State the blood parasite species.
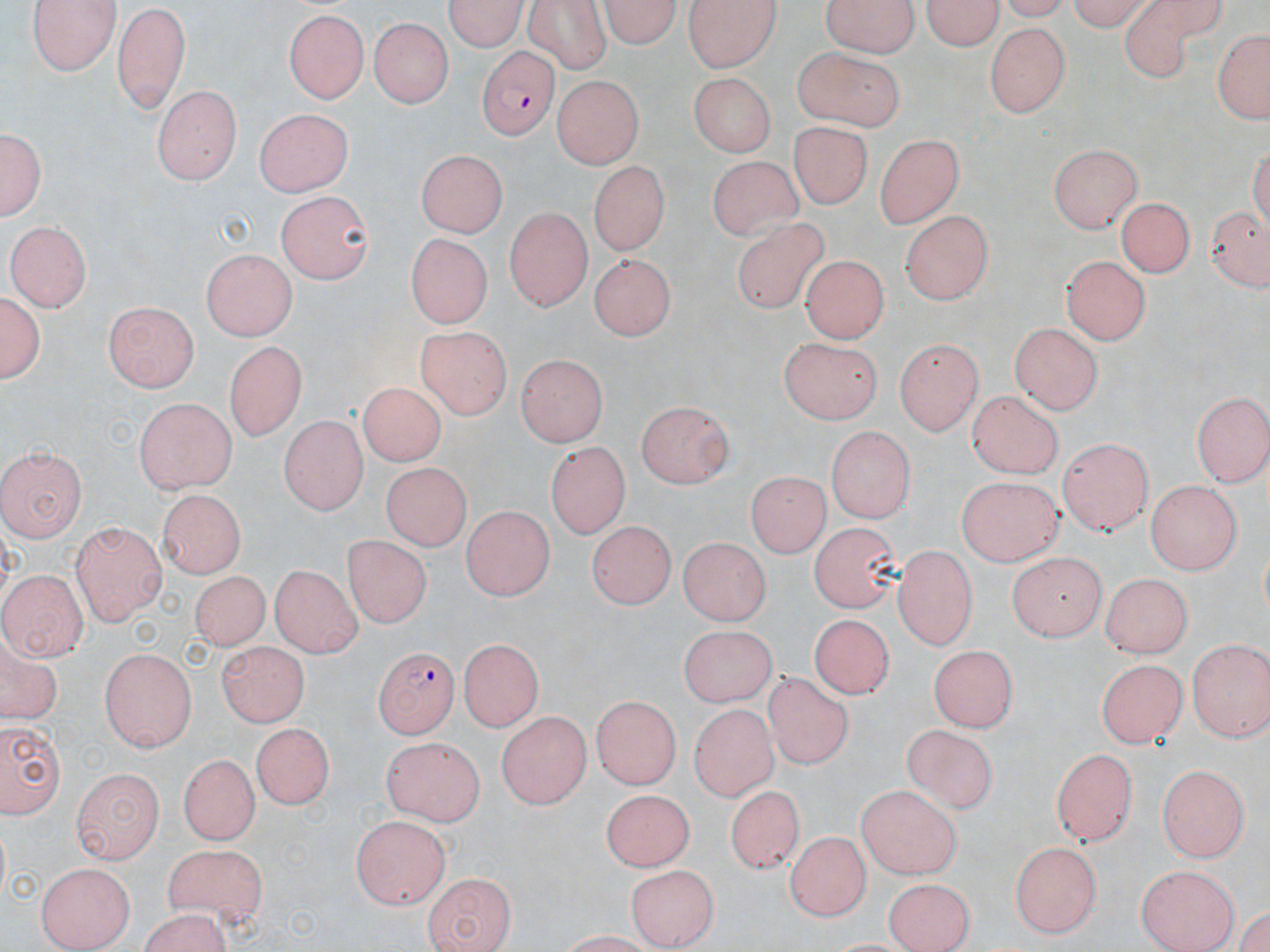
Plasmodium falciparum.

Approximate bounding boxes as (x1,y1)-(x2,y2) corner pairs in pixels. Plasmodium falciparum-infected red blood cell locations: (479,45)-(556,138), (371,644)-(458,740). Uninfected red blood cell locations: (27,0)-(121,73), (440,0)-(530,52), (598,0)-(684,49), (683,0)-(784,70), (824,0)-(916,58), (923,0)-(1006,52), (1063,0)-(1164,29), (1124,0)-(1228,83), (113,3)-(187,116), (521,3)-(613,71), (284,8)-(367,104), (368,16)-(453,107), (984,22)-(1066,117), (1211,26)-(1270,124), (795,45)-(908,128), (553,72)-(647,167), (686,73)-(775,160), (152,86)-(237,183), (254,109)-(356,198), (791,120)-(870,212), (2,127)-(47,223), (874,134)-(964,229), (1046,140)-(1145,231), (417,148)-(508,235), (707,153)-(809,243), (585,161)-(668,255), (274,194)-(374,282), (1117,197)-(1194,280), (1207,202)-(1270,290), (504,207)-(590,312), (902,210)-(995,299), (735,218)-(828,313), (7,220)-(92,310), (403,229)-(492,320), (585,246)-(669,335), (200,248)-(296,339), (801,254)-(888,340), (1061,254)-(1149,346), (1027,272)-(1132,394), (1,289)-(46,387), (106,301)-(198,391), (1009,323)-(1102,413), (414,326)-(512,422), (777,335)-(880,421), (897,337)-(981,435), (225,338)-(303,444), (514,354)-(609,444), (358,379)-(449,470), (966,388)-(1066,476), (1191,389)-(1270,483), (135,397)-(238,494), (636,401)-(736,487), (278,416)-(365,515), (823,427)-(919,524), (1058,438)-(1153,535), (547,443)-(628,539), (0,448)-(84,541), (383,463)-(474,552), (748,468)-(829,560), (958,476)-(1060,566), (1143,480)-(1243,573), (157,489)-(243,580), (460,502)-(549,602), (586,517)-(671,609), (810,517)-(899,608), (71,519)-(165,622), (342,532)-(430,628), (679,535)-(768,627), (894,547)-(976,648), (1004,547)-(1104,639), (269,563)-(361,660), (1,571)-(88,662), (189,571)-(263,654), (1103,571)-(1189,658), (812,616)-(897,700), (677,624)-(779,707), (456,637)-(541,731), (1184,637)-(1270,742), (0,639)-(60,728), (215,642)-(309,728), (929,643)-(1018,731), (100,648)-(198,752), (1094,656)-(1186,747), (763,671)-(855,769), (590,693)-(681,787), (689,702)-(787,802), (496,711)-(589,809), (0,715)-(67,818), (250,723)-(330,813), (902,725)-(1002,816), (378,735)-(487,826), (1052,745)-(1139,843), (179,752)-(260,840), (1156,765)-(1249,863), (72,767)-(164,861), (852,784)-(961,878), (727,788)-(804,873), (598,789)-(690,872), (352,816)-(451,908), (783,833)-(867,922), (1009,839)-(1100,937), (162,841)-(265,921), (34,862)-(136,947), (625,863)-(717,948), (1137,864)-(1238,952), (421,870)-(514,950), (885,876)-(974,952), (134,911)-(236,952). May-Grünwald-Giemsa stain. Light microscopy. Image is 1270×952 pixels. 1000x magnification. Thin blood smear. Single field of view.